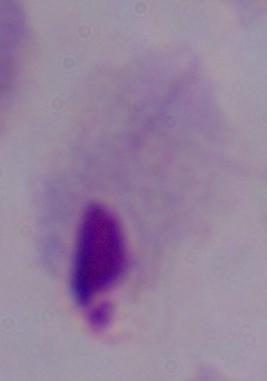

{
  "modality": "photomicrograph",
  "magnification": "1000x",
  "identification": "trichomonad"
}